Locate every Plasmodium parasite and every leukocyte.
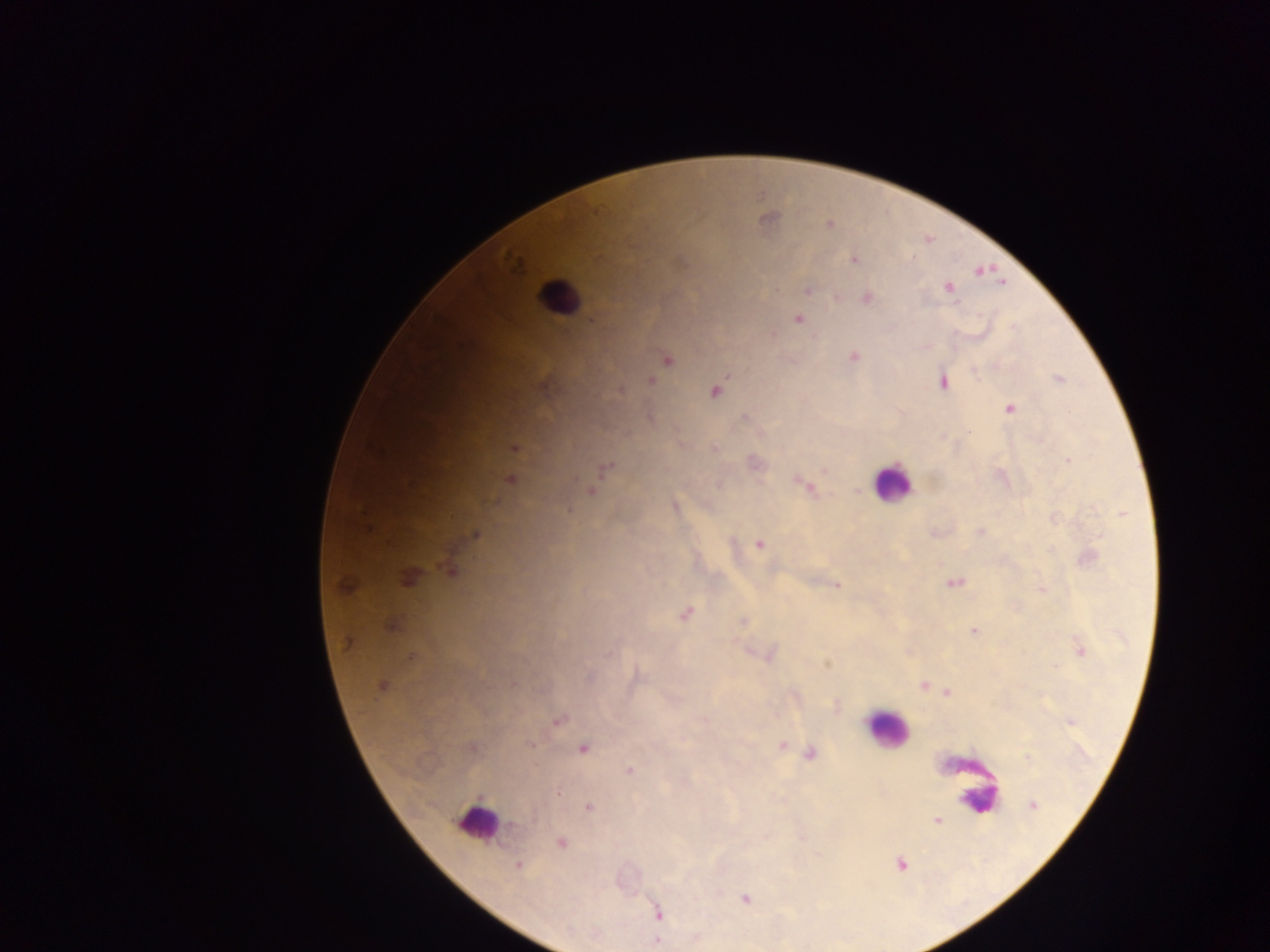

Approximate centers as {x, y} in pixels.
Plasmodium parasites: {767, 218}, {829, 225}, {854, 259}, {979, 270}, {1000, 282}, {947, 288}, {807, 290}, {867, 298}, {798, 319}, {591, 320}, {923, 345}, {853, 356}, {666, 359}, {1058, 379}, {651, 381}, {942, 382}, {620, 389}, {714, 391}, {1009, 409}, {744, 418}, {513, 447}, {714, 448}, {1068, 460}, {753, 463}, {605, 468}, {509, 479}, {719, 484}, {805, 485}, {590, 491}, {674, 507}, {567, 510}, {980, 531}, {935, 532}, {476, 534}, {759, 544}, {1087, 558}, {451, 571}, {409, 577}, {954, 583}, {836, 584}, {344, 585}, {1042, 589}, {684, 613}, {742, 621}, {392, 625}, {973, 630}, {348, 642}, {1079, 649}, {909, 652}, {769, 654}, {410, 657}, {826, 663}, {635, 677}, {588, 678}, {924, 685}, {381, 686}, {948, 692}, {835, 705}, {557, 720}, {780, 745}, {471, 748}, {583, 748}, {809, 754}, {629, 771}, {1032, 804}, {588, 807}, {936, 820}, {765, 836}, {560, 842}, {900, 863}, {518, 865}, {745, 899}, {658, 913}, {658, 933}, {695, 937}, {655, 941}.
Leukocytes: {558, 298}, {891, 482}, {886, 730}, {977, 786}, {979, 799}, {477, 821}.

preparation = thick blood smear
capture = mobile-phone photograph through a microscope
country = Ghana
image size = 1270×952 pixels
field of view = single